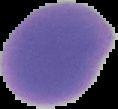

image size = 118×109 pixels
result = no Plasmodium parasites detected
preparation = thin blood smear
image type = segmented cell region with the area outside set to black